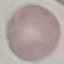
malaria status = uninfected
capture = smartphone camera at the microscope eyepiece
image type = cell patch, automatically extracted from a larger field of view and resized to 64 × 64 pixels
preparation = thin smear
stain = Giemsa